Report the malaria status of this cell.
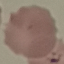

It is parasitized.

{
  "capture": "smartphone through the microscope eyepiece",
  "preparation": "thin blood film",
  "stain": "Giemsa",
  "image_type": "cell patch, automatically extracted from a larger field of view and resized to 64 × 64 pixels"
}